Outline each Babesia divergens-infected red blood cell.
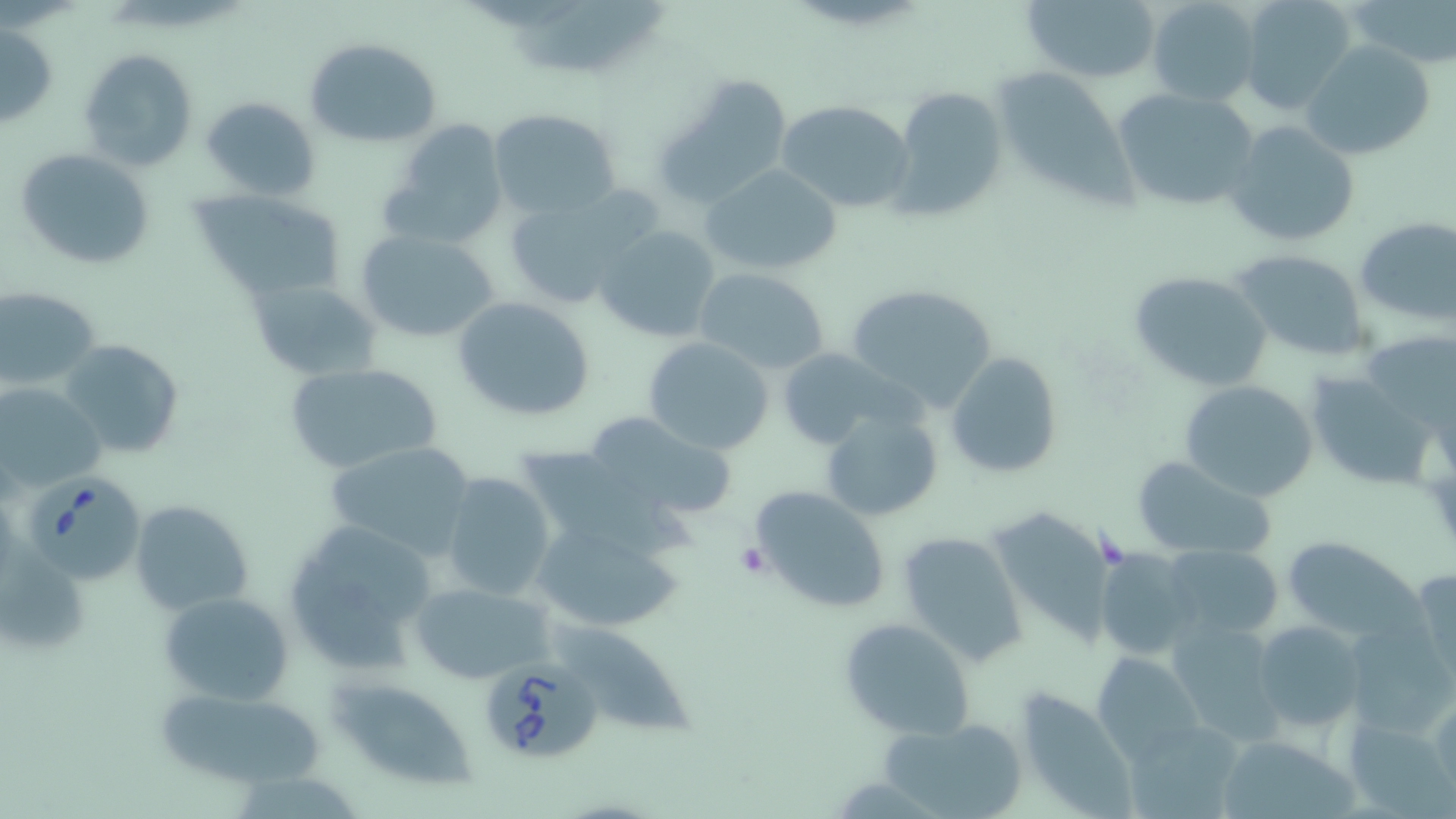

Approximate bounding boxes as (x1, y1, x2, y2) in pixels.
Babesia divergens-infected red blood cells: (23, 471, 145, 583), (475, 656, 606, 766).

slide_level_diagnosis: Babesia divergens
field_of_view: one of a larger specimen
modality: light microscopy
image_size: 1456×819 pixels
stain: May-Grünwald-Giemsa
preparation: thin blood smear
platelet_locations: 'approximate bounding boxes as (x1, y1, x2, y2) in pixels: (735, 543, 770, 578)'
magnification: 1000x
uninfected_red_blood_cell_locations: 'approximate bounding boxes as (x1, y1, x2, y2) in pixels: (513, 0, 665, 73), (1021, 0, 1162, 83), (1238, 0, 1355, 115), (1146, 2, 1262, 106), (1, 23, 57, 127), (303, 36, 444, 147), (1303, 42, 1435, 159), (77, 49, 198, 173), (653, 73, 795, 211), (891, 86, 1010, 220), (1113, 87, 1261, 213), (201, 96, 321, 200), (775, 100, 917, 214), (487, 107, 623, 220), (382, 118, 511, 251), (1225, 120, 1362, 248), (17, 148, 155, 271), (699, 162, 845, 276), (500, 186, 655, 310), (186, 189, 348, 299), (1354, 215, 1456, 329), (593, 225, 721, 343), (353, 229, 502, 345), (1231, 249, 1368, 360), (692, 267, 833, 377), (1128, 269, 1272, 393), (247, 277, 382, 381), (845, 282, 996, 414), (0, 287, 102, 390), (452, 295, 596, 421), (644, 337, 773, 456), (61, 338, 185, 458), (775, 348, 893, 445), (946, 352, 1063, 479), (282, 361, 445, 475), (1303, 370, 1441, 496), (1178, 380, 1319, 501), (0, 381, 105, 492), (821, 404, 943, 523), (579, 409, 739, 527), (322, 438, 480, 557), (1130, 455, 1278, 562), (438, 472, 554, 601), (751, 483, 891, 615), (129, 499, 255, 616), (989, 506, 1119, 649), (529, 517, 685, 635), (280, 518, 436, 671), (896, 529, 1028, 668), (1280, 536, 1426, 643), (1163, 543, 1284, 641), (1096, 548, 1198, 659), (1410, 563, 1456, 684), (410, 579, 552, 683), (159, 591, 295, 706), (838, 618, 974, 740), (1249, 619, 1365, 733), (1168, 621, 1282, 739), (561, 623, 702, 737), (1348, 623, 1454, 739), (1096, 653, 1202, 764), (329, 677, 478, 789), (152, 685, 329, 791), (1344, 716, 1454, 817), (883, 717, 1029, 819), (1218, 734, 1357, 817)'